Locate every blood parasite and identify its species.
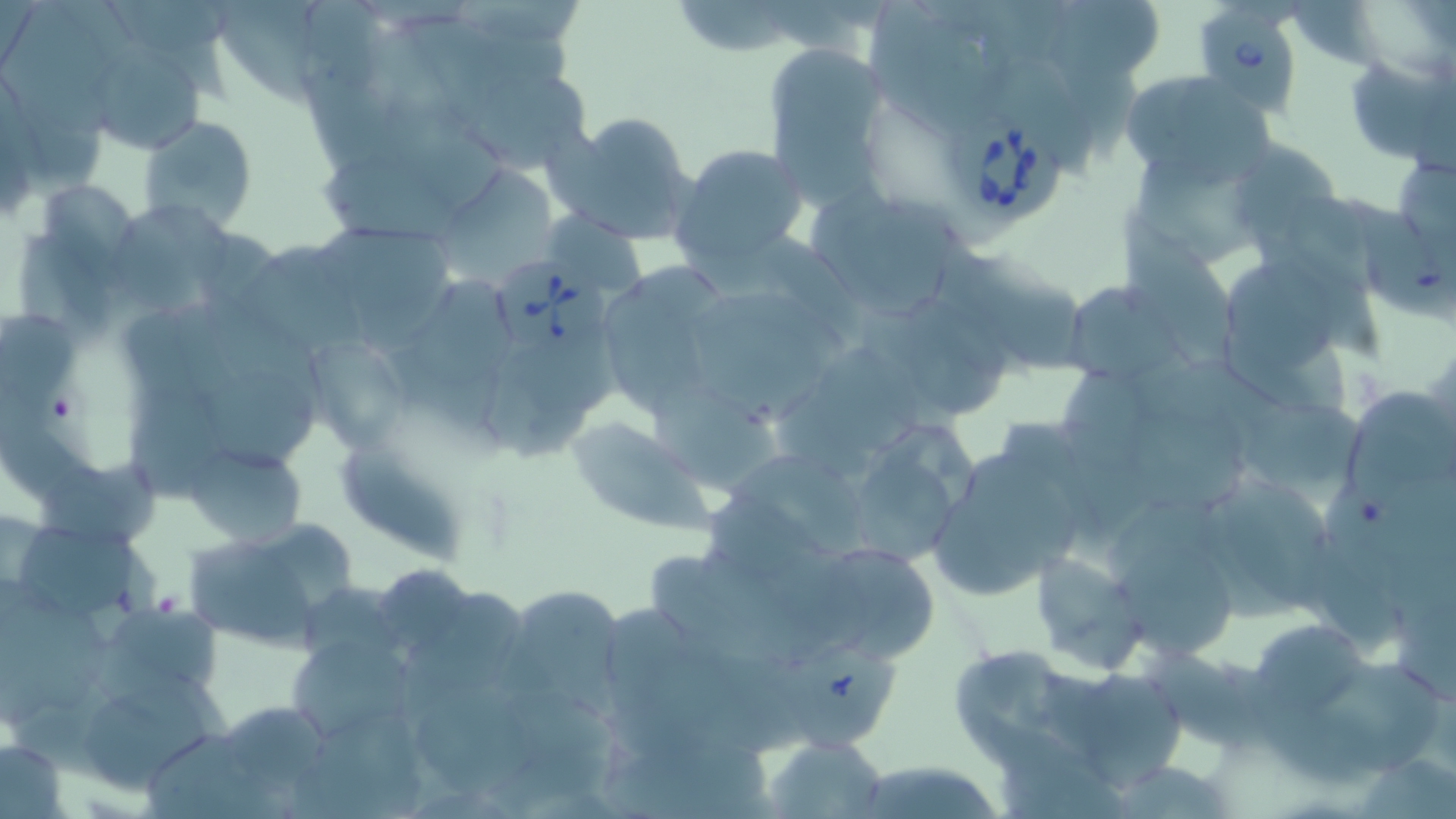
Approximate bounding boxes as [x1, y1, x2, y2] in pixels.
Babesia divergens-infected red blood cells: [1197, 7, 1299, 123], [941, 109, 1065, 228], [489, 254, 609, 372].
No Plasmodium falciparum, Plasmodium ovale, Plasmodium malariae, Plasmodium vivax, or Trypanosoma brucei observed.

Summary:
  - Uninfected red blood cell locations: [211, 1, 336, 107], [866, 5, 991, 134], [762, 43, 891, 211], [97, 52, 205, 153], [1344, 53, 1454, 165], [1119, 69, 1274, 184], [551, 111, 701, 245], [138, 113, 259, 233], [1224, 140, 1345, 250], [670, 142, 810, 273], [806, 190, 967, 316], [117, 208, 234, 308], [1121, 213, 1236, 363], [321, 231, 453, 336], [1229, 256, 1340, 374], [611, 259, 725, 418], [1059, 281, 1181, 385], [907, 297, 1005, 417], [688, 307, 824, 423], [303, 334, 407, 455], [777, 353, 918, 486], [1343, 383, 1454, 505], [1234, 392, 1369, 509], [566, 416, 704, 526], [929, 439, 1093, 602], [182, 442, 305, 548], [1192, 471, 1338, 620], [180, 522, 352, 651], [27, 530, 139, 615], [804, 539, 943, 663], [1029, 553, 1148, 675], [653, 556, 811, 667], [511, 586, 628, 716], [1248, 617, 1370, 720], [285, 635, 416, 746], [946, 644, 1090, 760], [1046, 667, 1195, 789], [88, 683, 209, 798], [765, 735, 888, 817], [0, 737, 66, 817], [848, 760, 1009, 819]
  - Slide-level diagnosis: Babesia divergens
  - Field of view: one of a larger specimen
  - Stain: May-Grünwald-Giemsa
  - Magnification: 1000x
  - Image size: 1456×819 pixels
  - Modality: optical microscopy
  - Preparation: thin blood smear